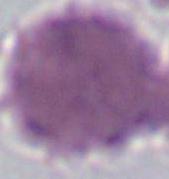 Photomicrograph. An erythrocyte is shown. 1000x magnification.